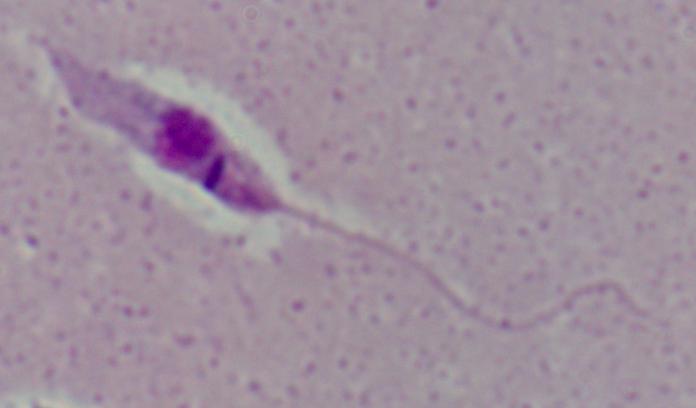
modality: micrograph
magnification: 1000x
identification: Leishmania